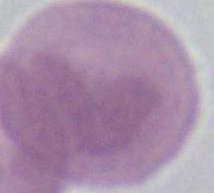

identification = red blood cell
magnification = 1000x
modality = photomicrograph